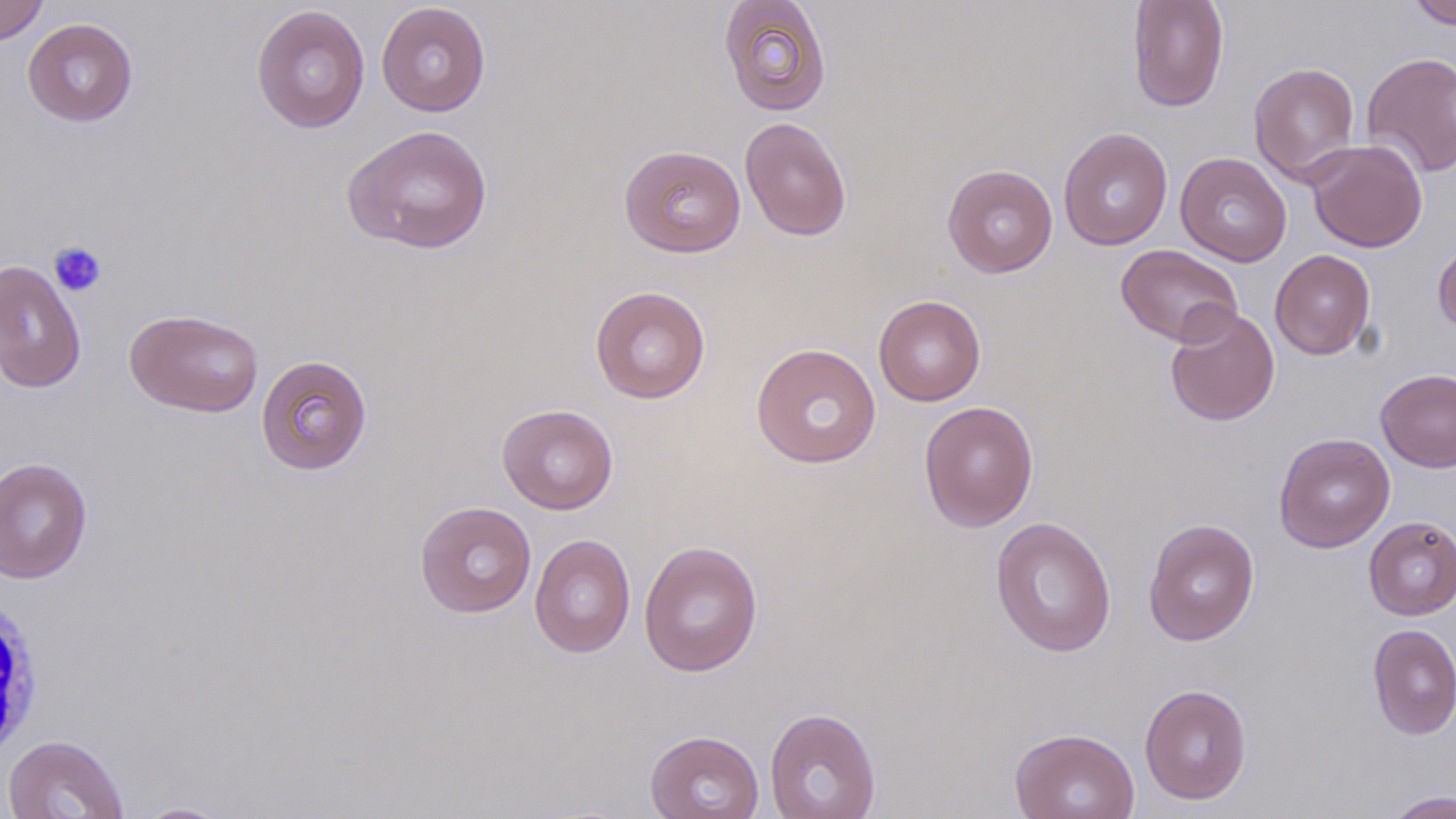

Approximate bounding boxes as named x1/y1/x2/y2 corners in pixels. White blood cell locations: (x1=0, y1=598, x2=44, y2=762). Uninfected red blood cell locations: (x1=1127, y1=0, x2=1228, y2=112), (x1=1407, y1=0, x2=1455, y2=29), (x1=0, y1=1, x2=49, y2=45), (x1=718, y1=1, x2=831, y2=117), (x1=376, y1=2, x2=491, y2=117), (x1=251, y1=5, x2=370, y2=133), (x1=23, y1=18, x2=138, y2=127), (x1=1360, y1=51, x2=1456, y2=178), (x1=1248, y1=61, x2=1361, y2=185), (x1=739, y1=116, x2=852, y2=241), (x1=342, y1=124, x2=494, y2=255), (x1=1058, y1=127, x2=1173, y2=251), (x1=1306, y1=139, x2=1427, y2=252), (x1=619, y1=145, x2=746, y2=258), (x1=1175, y1=152, x2=1292, y2=267), (x1=942, y1=163, x2=1058, y2=278), (x1=1433, y1=239, x2=1456, y2=335), (x1=1116, y1=244, x2=1243, y2=347), (x1=1270, y1=249, x2=1376, y2=360), (x1=0, y1=260, x2=87, y2=394), (x1=589, y1=286, x2=710, y2=404), (x1=873, y1=295, x2=986, y2=407), (x1=1164, y1=306, x2=1280, y2=426), (x1=125, y1=309, x2=264, y2=417), (x1=751, y1=343, x2=882, y2=469), (x1=256, y1=354, x2=373, y2=475), (x1=1374, y1=368, x2=1456, y2=473), (x1=918, y1=400, x2=1039, y2=532), (x1=497, y1=404, x2=618, y2=514), (x1=1273, y1=433, x2=1395, y2=552), (x1=0, y1=457, x2=92, y2=583), (x1=414, y1=500, x2=536, y2=618), (x1=990, y1=516, x2=1117, y2=657), (x1=1363, y1=516, x2=1456, y2=620), (x1=1142, y1=518, x2=1260, y2=645), (x1=529, y1=534, x2=636, y2=658), (x1=639, y1=539, x2=763, y2=677), (x1=1367, y1=623, x2=1456, y2=740), (x1=1139, y1=683, x2=1251, y2=805), (x1=764, y1=707, x2=881, y2=819), (x1=1009, y1=727, x2=1140, y2=819), (x1=644, y1=730, x2=764, y2=819), (x1=2, y1=735, x2=129, y2=819), (x1=1383, y1=790, x2=1456, y2=819), (x1=132, y1=802, x2=234, y2=818). Platelet locations: (x1=49, y1=241, x2=107, y2=297). Slide-level diagnosis: no evidence of blood parasites. Single field of view. Optical microscopy. May-Grünwald-Giemsa-stained preparation. Image is 1456×819 pixels. Thin blood film. 1000x magnification.